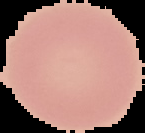
result = negative for Plasmodium parasites
image size = 145×133 pixels
image type = segmented cell region with the area outside set to black
preparation = thin blood smear